Locate every malaria parasite.
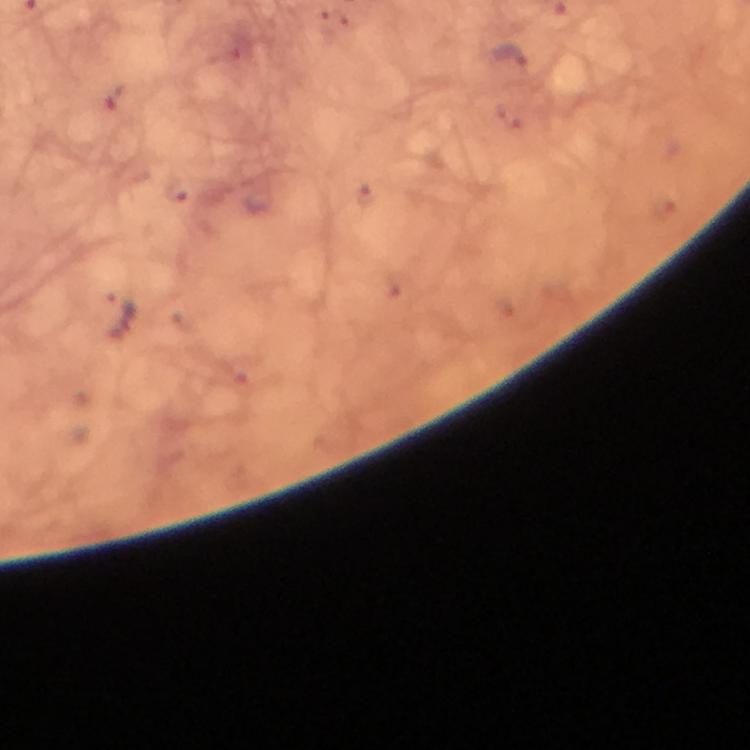
Approximate centers as (x, y) in pixels.
Malaria parasites: (122, 313).

Smartphone photograph taken through a microscope. Image is 750×750 pixels. Thick blood film. At 100x magnification. Giemsa-stained preparation. From a diagnostic examination for malaria. Cropped region of a single field of view. Immersion oil applied.